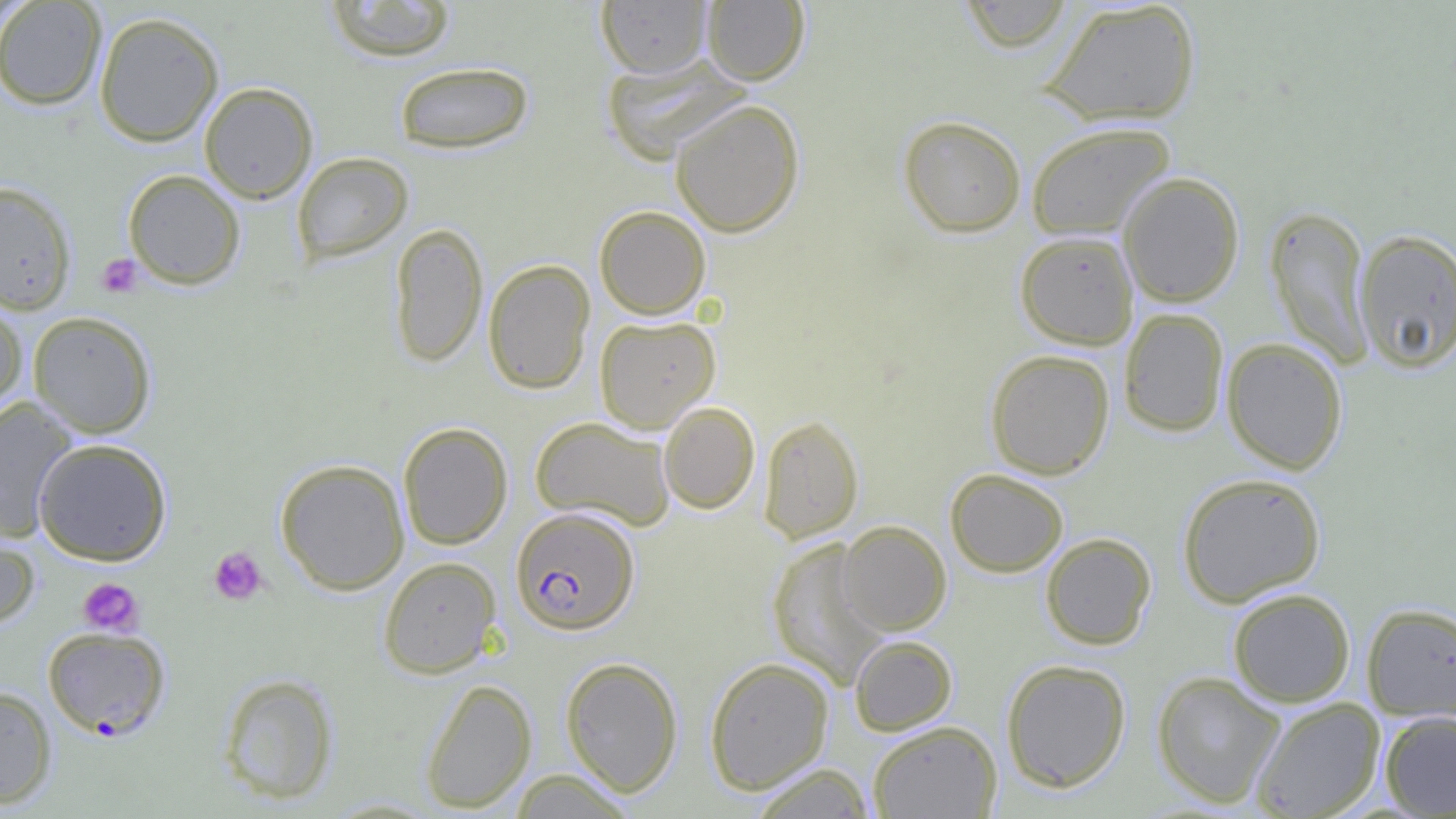

slide_level_diagnosis: Plasmodium falciparum
modality: light microscopy
preparation: thin blood smear
image_size: 1456×819 pixels
platelet_locations: 'approximate bounding boxes as named x1/y1/x2/y2 corners in pixels: (x1=95, y1=254, x2=143, y2=298), (x1=208, y1=546, x2=268, y2=605), (x1=78, y1=578, x2=144, y2=636)'
plasmodium_falciparum_infected_red_blood_cell_locations: 'approximate bounding boxes as named x1/y1/x2/y2 corners in pixels: (x1=510, y1=507, x2=639, y2=635), (x1=43, y1=626, x2=170, y2=740)'
uninfected_red_blood_cell_locations: 'approximate bounding boxes as named x1/y1/x2/y2 corners in pixels: (x1=596, y1=0, x2=712, y2=77), (x1=702, y1=0, x2=810, y2=85), (x1=957, y1=0, x2=1076, y2=53), (x1=0, y1=1, x2=107, y2=110), (x1=324, y1=1, x2=457, y2=61), (x1=1040, y1=1, x2=1202, y2=126), (x1=94, y1=11, x2=224, y2=147), (x1=601, y1=52, x2=751, y2=165), (x1=394, y1=61, x2=534, y2=154), (x1=199, y1=82, x2=317, y2=203), (x1=670, y1=99, x2=805, y2=236), (x1=898, y1=115, x2=1027, y2=237), (x1=1025, y1=121, x2=1175, y2=240), (x1=292, y1=151, x2=413, y2=264), (x1=123, y1=169, x2=246, y2=289), (x1=1118, y1=172, x2=1245, y2=307), (x1=0, y1=180, x2=77, y2=315), (x1=595, y1=206, x2=711, y2=320), (x1=1265, y1=206, x2=1374, y2=368), (x1=390, y1=222, x2=488, y2=367), (x1=1353, y1=228, x2=1456, y2=373), (x1=1015, y1=230, x2=1139, y2=350), (x1=482, y1=258, x2=595, y2=394), (x1=0, y1=298, x2=28, y2=417), (x1=1118, y1=308, x2=1229, y2=437), (x1=27, y1=311, x2=157, y2=438), (x1=594, y1=315, x2=721, y2=433), (x1=1221, y1=337, x2=1348, y2=474), (x1=986, y1=349, x2=1115, y2=479), (x1=0, y1=397, x2=79, y2=541), (x1=659, y1=402, x2=760, y2=514), (x1=657, y1=409, x2=863, y2=522), (x1=758, y1=414, x2=864, y2=542), (x1=531, y1=416, x2=676, y2=532), (x1=398, y1=422, x2=513, y2=550), (x1=33, y1=438, x2=172, y2=565), (x1=275, y1=459, x2=410, y2=595), (x1=945, y1=468, x2=1069, y2=577), (x1=1177, y1=472, x2=1327, y2=607), (x1=838, y1=520, x2=952, y2=635), (x1=0, y1=524, x2=40, y2=630), (x1=1040, y1=532, x2=1156, y2=650), (x1=767, y1=537, x2=890, y2=690), (x1=378, y1=556, x2=502, y2=678), (x1=1227, y1=588, x2=1356, y2=707), (x1=1360, y1=602, x2=1456, y2=721), (x1=849, y1=635, x2=957, y2=736), (x1=560, y1=656, x2=684, y2=796), (x1=704, y1=657, x2=834, y2=794), (x1=1001, y1=659, x2=1132, y2=793), (x1=1151, y1=671, x2=1285, y2=808), (x1=217, y1=673, x2=339, y2=805), (x1=420, y1=678, x2=537, y2=813), (x1=0, y1=685, x2=57, y2=809), (x1=1250, y1=697, x2=1386, y2=819), (x1=1379, y1=711, x2=1456, y2=818), (x1=868, y1=720, x2=1002, y2=818), (x1=747, y1=763, x2=876, y2=819), (x1=508, y1=770, x2=638, y2=818)'
magnification: 1000x
field_of_view: single